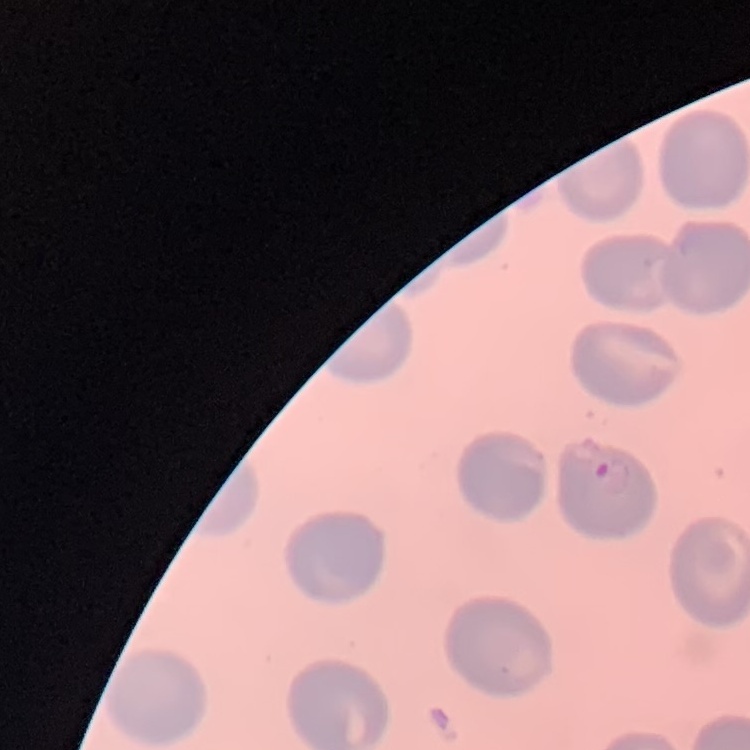

Summary:
  - Erythrocyte morphology: no rouleaux formation
  - Image type: square crop of a larger photomicrograph
  - Stain: Field's or Giemsa
  - Preparation: thin blood film